Identify the preparation type.
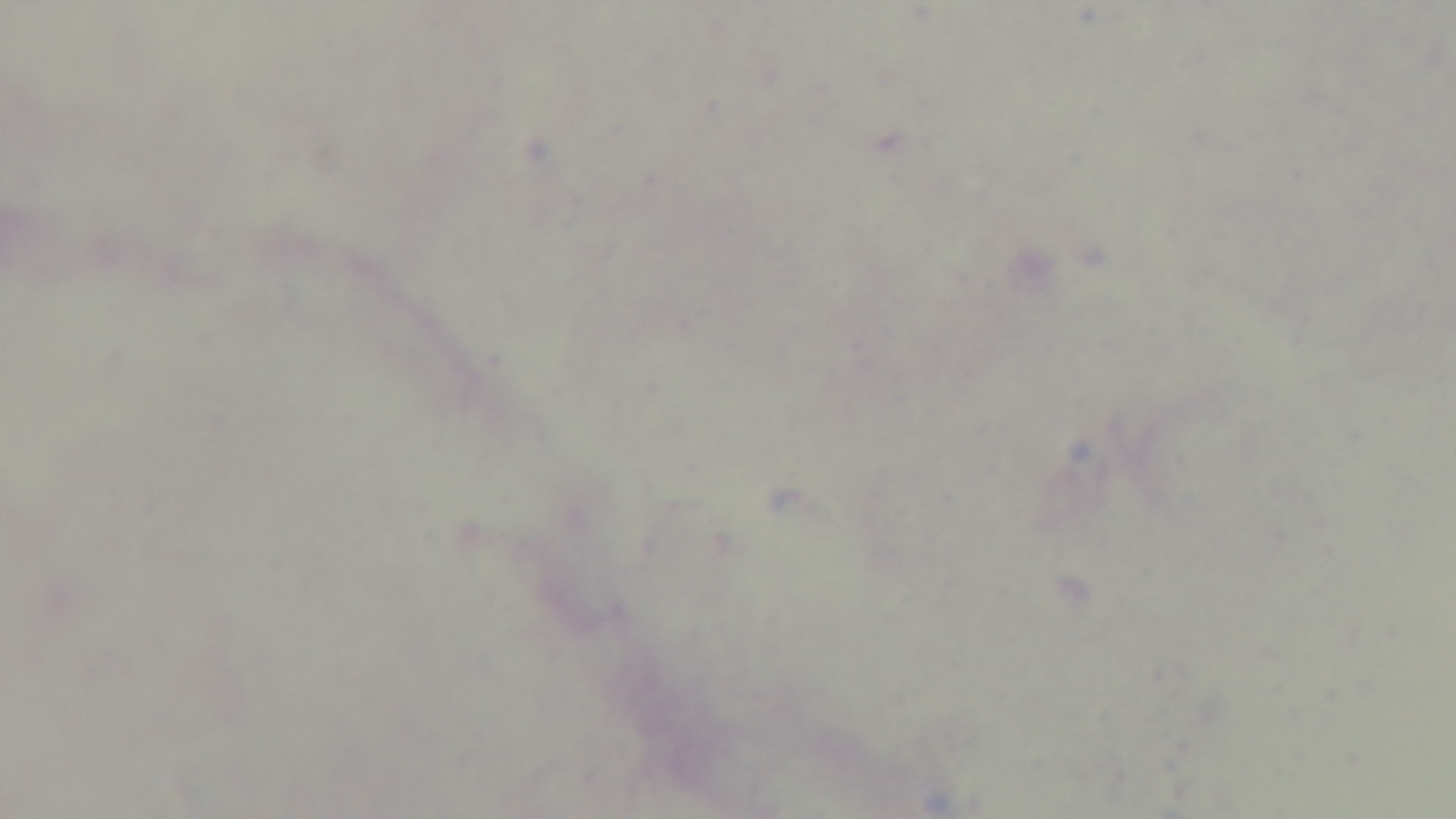
It is a thick blood film.

field of view = one from the slide
modality = light microscopy
malaria status = negative
objective = 100x oil immersion
capture = mounted 4K digital camera
stain = Giemsa